Classify this cell by malaria status.
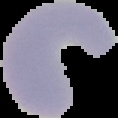
It is uninfected.

Summary:
  - Image size: 118×118 pixels
  - Preparation: thin blood smear
  - Image type: cell region segmented out of the field of view; surrounding area masked to black